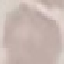

malaria status = uninfected
capture = smartphone through the microscope eyepiece
image type = cell patch, automatically extracted from a larger field of view and resized to 64 × 64 pixels
stain = Giemsa
preparation = thin smear